Locate every Plasmodium parasite and every leukocyte.
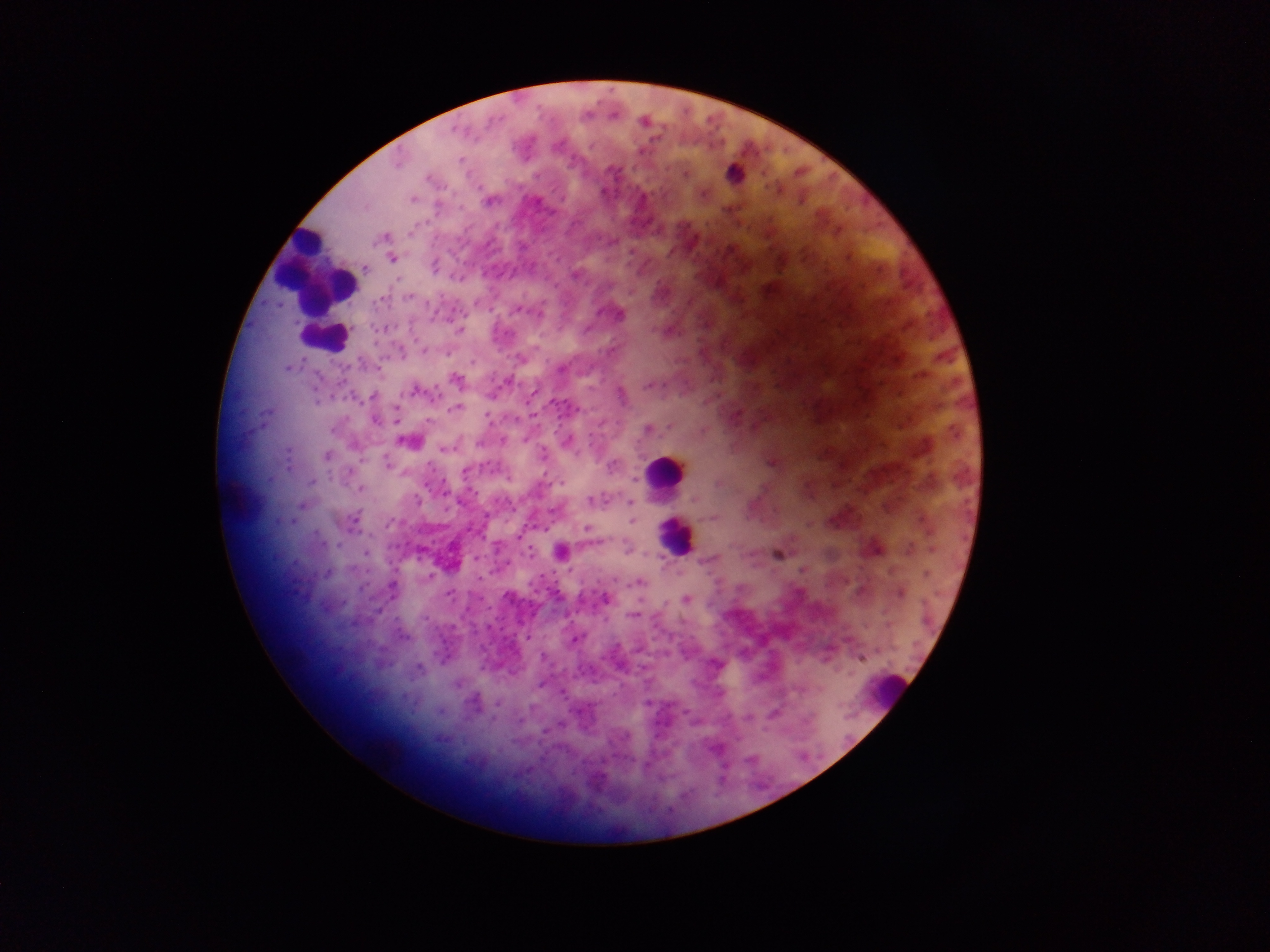

Approximate centers as {x, y} in pixels.
Plasmodium parasites: {644, 121}, {456, 130}, {460, 160}, {398, 164}, {733, 173}, {685, 174}, {429, 179}, {703, 195}, {412, 198}, {491, 201}, {383, 237}, {612, 241}, {392, 258}, {434, 266}, {366, 268}, {575, 276}, {408, 297}, {519, 310}, {619, 315}, {459, 331}, {424, 350}, {521, 359}, {472, 362}, {290, 367}, {561, 369}, {457, 380}, {506, 383}, {648, 386}, {414, 391}, {373, 396}, {622, 397}, {317, 401}, {555, 404}, {455, 408}, {398, 410}, {488, 417}, {375, 420}, {428, 422}, {333, 429}, {648, 429}, {407, 442}, {444, 449}, {543, 454}, {327, 455}, {771, 462}, {387, 463}, {612, 465}, {465, 471}, {311, 482}, {561, 483}, {361, 489}, {418, 500}, {591, 501}, {694, 501}, {631, 502}, {713, 517}, {354, 519}, {391, 522}, {632, 522}, {587, 529}, {518, 535}, {337, 545}, {627, 548}, {561, 551}, {366, 552}, {531, 553}, {777, 555}, {476, 559}, {709, 560}, {327, 573}, {926, 574}, {479, 578}, {637, 582}, {393, 586}, {448, 594}, {900, 594}, {605, 598}, {687, 600}, {633, 615}, {425, 619}, {888, 625}, {402, 636}, {527, 637}, {575, 640}, {543, 657}, {861, 658}, {716, 665}, {418, 667}, {562, 693}, {497, 703}, {774, 714}, {748, 718}.
Leukocytes: {318, 272}, {322, 336}, {666, 471}, {675, 535}, {887, 690}.

image size = 1270×952 pixels
field of view = single
country = Ghana
preparation = thick blood smear
capture = mobile-phone photograph through a microscope